State which parasite is depicted.
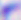
Toxoplasma gondii.

magnification = 400x
modality = micrograph